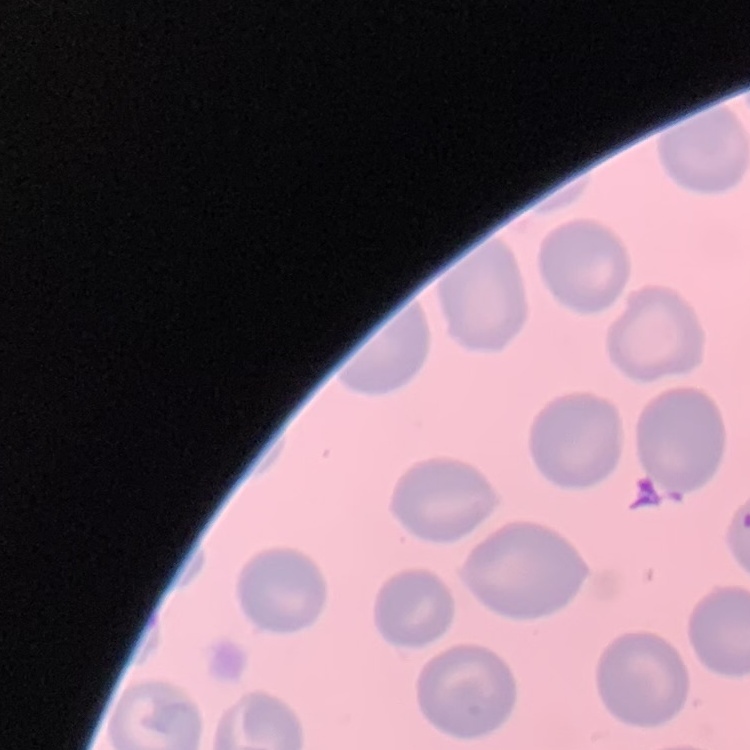

Summary:
  - Red blood cell morphology: no rouleaux formation
  - Preparation: thin blood smear
  - Image type: one tile cut from a larger photomicrograph
  - Stain: Field's or Giemsa